Identify the blood parasite species.
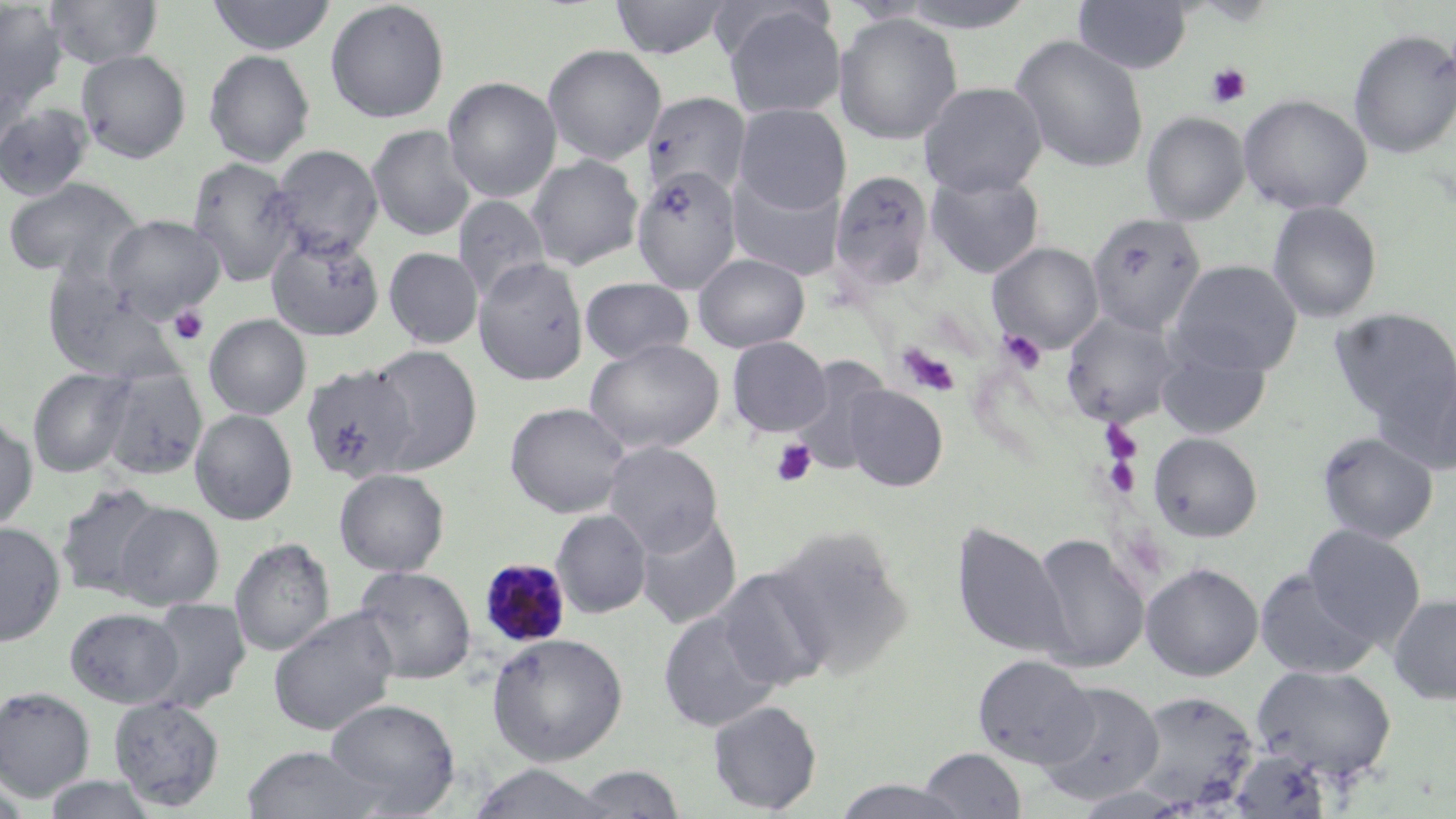

Plasmodium malariae.

Approximate bounding boxes as (x1,y1)-(x2,y2) corner pairs in pixels. Platelet locations: (1204,64)-(1251,108), (168,305)-(210,346), (998,330)-(1046,373), (896,343)-(960,397), (1102,422)-(1143,467), (770,438)-(818,487), (1102,453)-(1143,497). Plasmodium malariae-infected red blood cell locations: (480,558)-(572,647). Uninfected red blood cell locations: (45,0)-(163,69), (207,0)-(337,56), (325,0)-(450,124), (611,0)-(733,59), (891,0)-(1041,33), (1073,0)-(1192,75), (0,2)-(68,113), (720,5)-(846,119), (833,12)-(963,146), (1348,29)-(1456,159), (1011,35)-(1149,173), (542,44)-(667,165), (76,49)-(191,163), (203,49)-(315,167), (442,76)-(562,203), (918,81)-(1049,197), (642,91)-(752,200), (1238,94)-(1373,215), (734,103)-(850,214), (0,104)-(94,201), (1141,112)-(1250,225), (367,124)-(476,241), (269,145)-(383,260), (526,155)-(643,272), (187,156)-(301,286), (631,166)-(742,293), (828,169)-(936,297), (924,170)-(1045,279), (727,171)-(846,282), (2,178)-(143,281), (452,195)-(551,303), (1267,201)-(1383,324), (1086,212)-(1207,337), (103,215)-(224,321), (265,233)-(384,341), (987,242)-(1104,354), (384,247)-(483,348), (694,253)-(810,352), (474,258)-(589,385), (1168,260)-(1303,376), (41,262)-(185,385), (580,277)-(694,365), (1330,308)-(1456,428), (1061,312)-(1182,426), (204,314)-(311,420), (726,336)-(832,438), (584,338)-(724,453), (1156,341)-(1272,439), (365,345)-(482,474), (788,358)-(892,477), (1381,359)-(1456,476), (97,365)-(208,480), (300,365)-(417,483), (28,367)-(135,478), (842,384)-(948,492), (505,402)-(630,518), (190,409)-(297,525), (0,414)-(38,533), (1316,431)-(1439,544), (1148,432)-(1264,542), (603,441)-(723,555), (334,468)-(450,576), (55,483)-(168,601), (114,503)-(223,610), (551,509)-(651,618), (635,509)-(742,630), (0,521)-(65,646), (952,521)-(1071,660), (767,524)-(914,680), (1303,525)-(1426,647), (1029,534)-(1150,672), (230,537)-(335,657), (1141,562)-(1264,681), (353,566)-(476,685), (714,566)-(835,691), (1254,569)-(1379,679), (1388,594)-(1456,705), (141,598)-(250,714), (65,607)-(184,708), (269,608)-(399,737), (659,609)-(782,732), (487,632)-(629,765), (973,654)-(1096,769), (1251,663)-(1397,782), (1035,680)-(1165,805), (0,686)-(95,801), (1130,690)-(1258,810), (108,696)-(226,811), (325,698)-(460,814), (707,700)-(822,814), (241,745)-(389,819), (918,747)-(1027,819), (467,763)-(617,818), (570,764)-(687,818), (41,774)-(161,818), (0,778)-(34,819), (832,778)-(967,819). Optical microscopy. Thin blood film. Image is 1456×819 pixels. May-Grünwald-Giemsa-stained preparation. Single field of view. Captured at 1000x magnification.